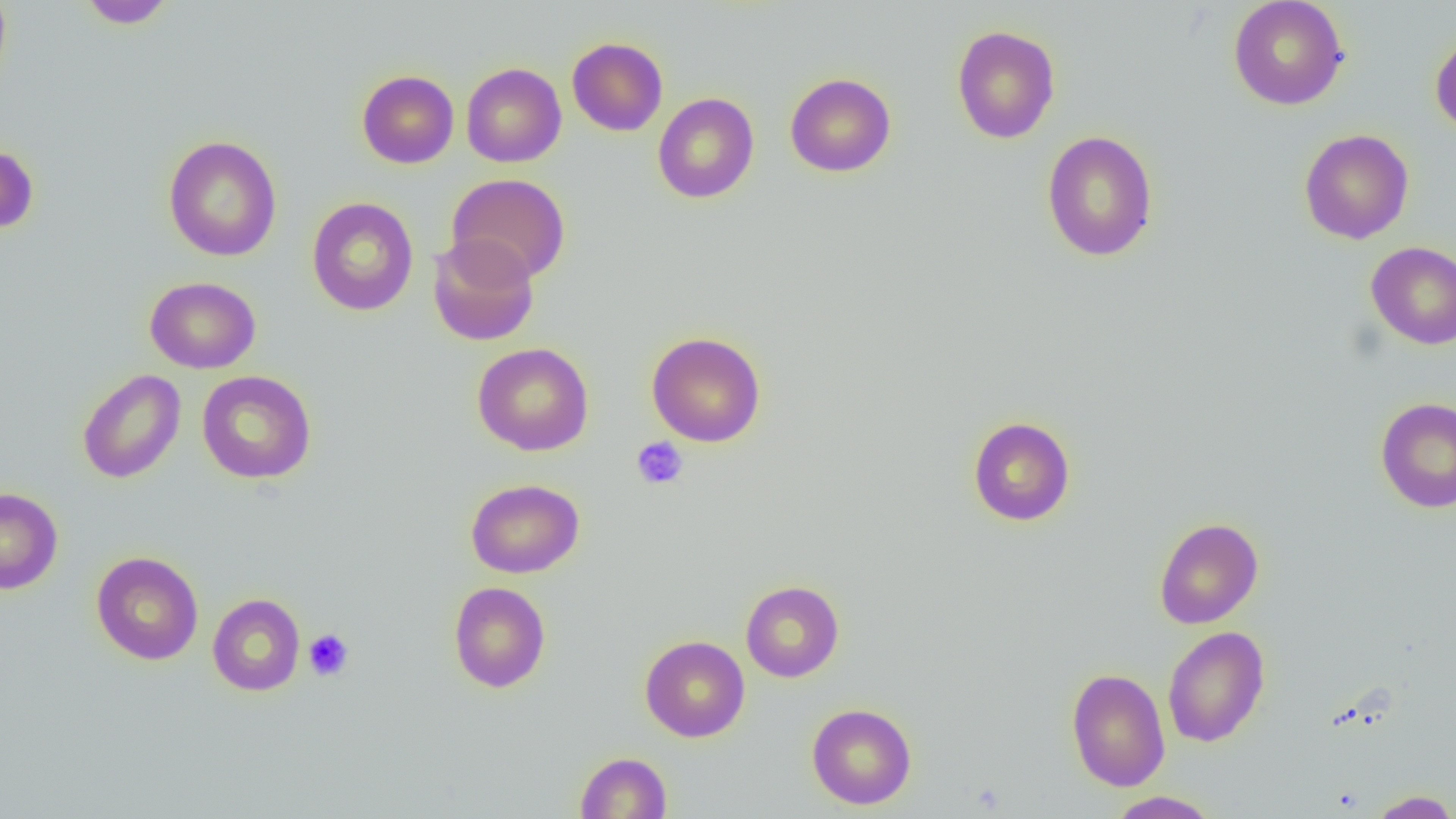
slide-level diagnosis = negative for blood parasites
magnification = 1000x
modality = light microscopy
platelet locations = approximate bounding boxes as (x1,y1)-(x2,y2) corner pairs in pixels: (631,436)-(689,489), (303,629)-(354,681)
uninfected red blood cell locations = approximate bounding boxes as (x1,y1)-(x2,y2) corner pairs in pixels: (0,0)-(12,91), (77,0)-(177,29), (1228,0)-(1349,110), (951,25)-(1060,143), (1430,30)-(1456,138), (567,37)-(668,136), (461,62)-(566,167), (356,69)-(459,169), (785,73)-(896,177), (652,92)-(759,203), (1299,128)-(1414,244), (1041,130)-(1159,262), (163,135)-(282,262), (0,142)-(39,236), (445,174)-(570,284), (306,197)-(419,315), (427,235)-(540,346), (1365,241)-(1456,350), (145,276)-(261,373), (647,331)-(767,447), (471,342)-(594,456), (77,369)-(185,484), (197,370)-(316,484), (1375,396)-(1456,513), (967,416)-(1076,526), (465,478)-(584,578), (0,487)-(63,595), (1154,517)-(1264,629), (91,551)-(203,665), (740,580)-(844,682), (448,581)-(551,693), (207,593)-(305,696), (1162,626)-(1270,747), (639,635)-(750,742), (1066,667)-(1170,792), (806,703)-(917,809), (575,751)-(672,818), (1366,790)-(1456,818), (1106,791)-(1221,818)
field of view = single
preparation = thin blood smear
image size = 1456×819 pixels